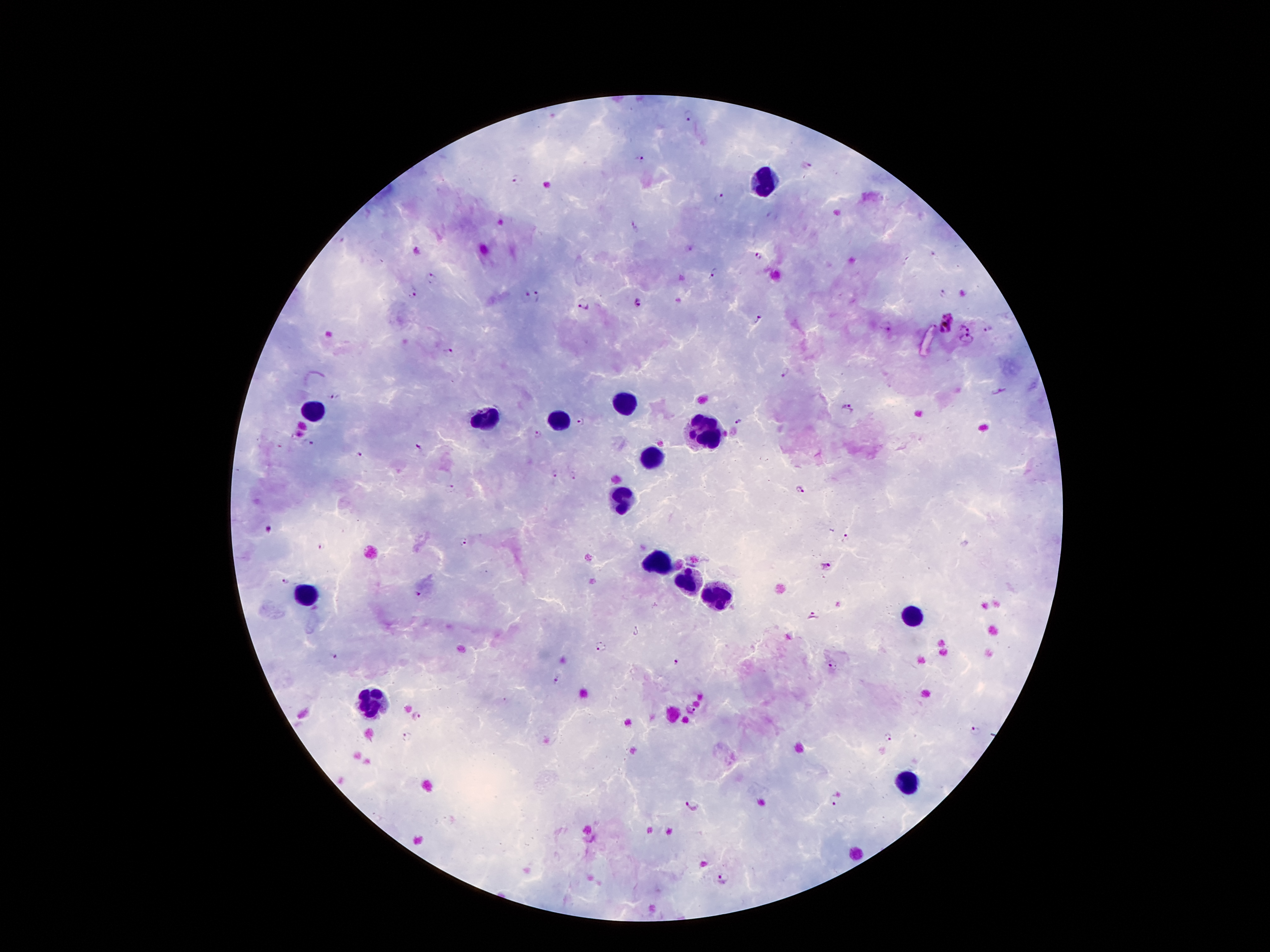

coordinate format = approximate centers as {x, y} in pixels
leukocyte locations = {765, 182}, {624, 400}, {312, 410}, {488, 418}, {563, 418}, {707, 433}, {652, 457}, {624, 499}, {656, 562}, {686, 581}, {306, 594}, {716, 599}, {912, 615}, {372, 702}, {907, 783}
malaria parasite locations = {688, 118}, {642, 159}, {808, 165}, {518, 179}, {718, 198}, {635, 228}, {418, 253}, {758, 258}, {716, 274}, {433, 277}, {945, 293}, {412, 294}, {539, 295}, {525, 297}, {637, 302}, {586, 305}, {759, 319}, {946, 322}, {886, 327}, {968, 327}, {989, 330}, {967, 341}, {447, 351}, {787, 371}, {999, 390}, {335, 395}, {847, 407}, {580, 423}, {741, 423}, {538, 434}, {298, 436}, {313, 443}, {418, 450}, {357, 454}, {554, 473}, {573, 477}, {452, 489}, {801, 490}, {269, 530}, {845, 536}, {464, 541}, {322, 547}, {825, 565}, {285, 581}, {415, 594}, {813, 617}, {600, 646}, {335, 657}, {678, 663}, {832, 666}, {557, 680}, {689, 710}, {417, 716}, {974, 731}, {887, 736}, {407, 739}, {835, 800}, {691, 805}, {722, 877}
image size = 1270×952 pixels
stain = Giemsa
preparation = thick blood film
magnification = 100x
capture = smartphone camera through the microscope eyepiece
patient malaria status = infected with Plasmodium falciparum
field of view = single